Classify this cell by malaria status.
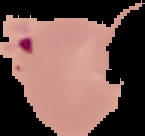

Parasitized.

Summary:
  - Image type: cell region segmented out of the field of view; surrounding area masked to black
  - Image size: 145×136 pixels
  - Preparation: thin blood smear